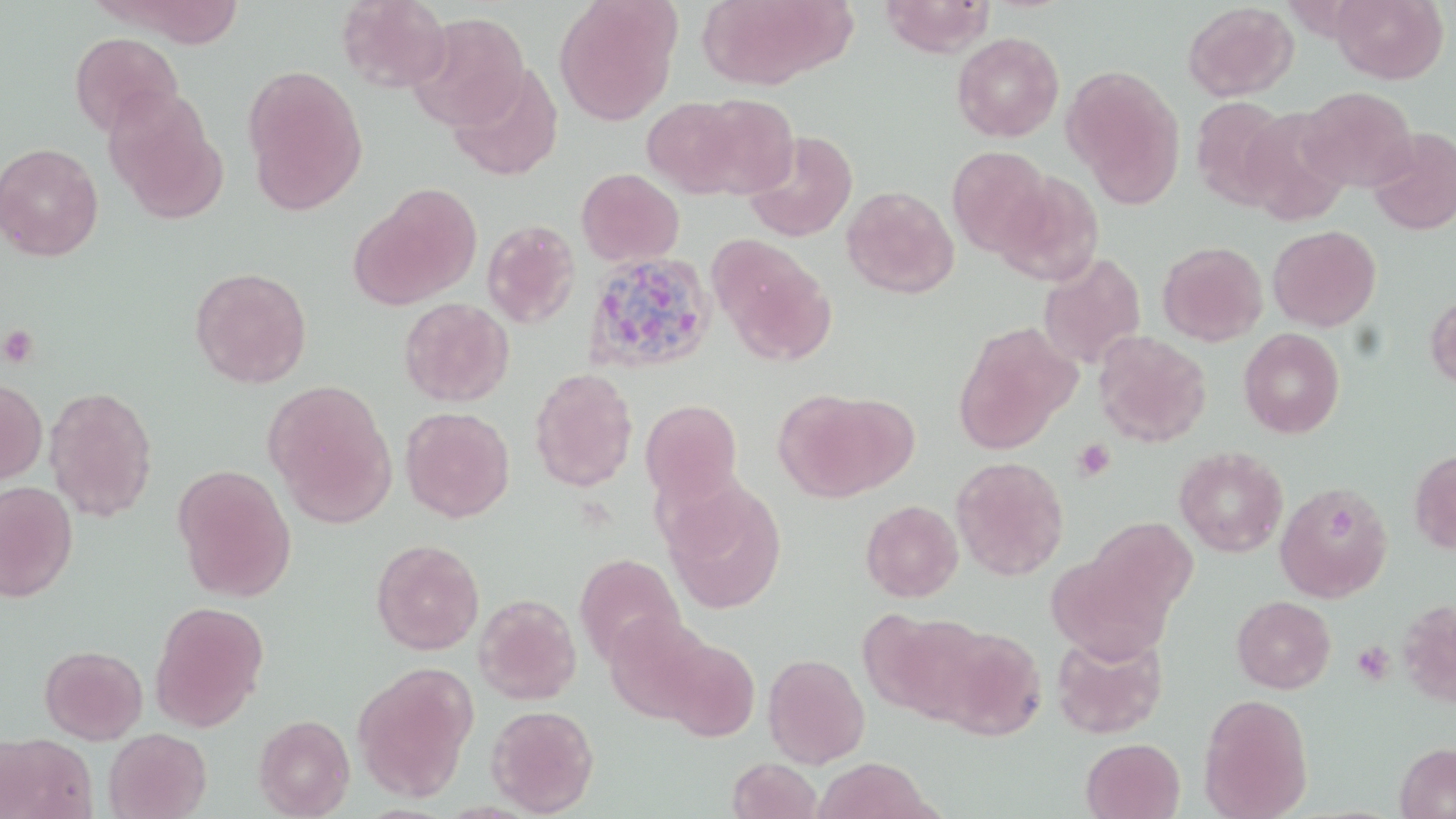

{
  "slide_level_diagnosis": "Plasmodium ovale",
  "platelet_locations": "approximate bounding boxes as (x1,y1)-(x2,y2) corner pairs in pixels: (0,325)-(38,368), (1072,439)-(1115,482), (1351,642)-(1393,685)",
  "stain": "May-Grünwald-Giemsa",
  "magnification": "1000x",
  "modality": "light microscopy",
  "field_of_view": "single",
  "preparation": "thin blood film",
  "image_size": "1456×819 pixels",
  "uninfected_red_blood_cell_locations": "approximate bounding boxes as (x1,y1)-(x2,y2) corner pairs in pixels: (103,0)-(247,48), (336,0)-(452,92), (553,0)-(681,126), (694,0)-(848,89), (880,0)-(996,57), (1331,0)-(1449,85), (1182,2)-(1298,101), (409,11)-(530,132), (70,32)-(183,137), (952,32)-(1064,142), (241,64)-(369,216), (447,64)-(564,182), (1062,64)-(1186,206), (1298,86)-(1418,193), (103,88)-(228,225), (685,94)-(800,198), (639,96)-(754,198), (1190,96)-(1293,209), (1237,108)-(1353,225), (1368,129)-(1456,237), (742,130)-(859,242), (0,142)-(104,261), (945,146)-(1054,259), (576,168)-(684,266), (994,173)-(1104,286), (351,184)-(482,310), (841,185)-(960,299), (481,219)-(582,329), (1267,225)-(1381,332), (707,234)-(834,363), (1157,241)-(1268,346), (1038,253)-(1147,370), (190,266)-(312,389), (1424,290)-(1456,391), (399,296)-(515,407), (952,323)-(1079,454), (1239,327)-(1345,438), (1093,331)-(1213,447), (529,367)-(638,492), (0,377)-(47,488), (263,379)-(399,528), (44,385)-(159,522), (773,389)-(910,502), (640,399)-(743,503), (400,406)-(515,523), (1174,445)-(1289,557), (1409,447)-(1456,554), (950,456)-(1070,581), (171,463)-(297,603), (0,480)-(78,602), (1275,480)-(1394,602), (662,481)-(788,614), (860,499)-(963,602), (1085,517)-(1197,624), (371,539)-(485,655), (1046,552)-(1175,665), (574,554)-(687,668), (474,594)-(582,705), (1231,595)-(1336,694), (1397,598)-(1456,708), (149,600)-(269,732), (859,610)-(988,723), (604,614)-(715,724), (927,623)-(1047,741), (1051,630)-(1168,740), (658,636)-(760,742), (40,645)-(147,744), (763,653)-(870,768), (352,661)-(478,803), (1198,693)-(1314,819), (486,704)-(600,816), (253,714)-(355,818), (104,727)-(212,819), (1,732)-(97,819), (1081,737)-(1185,819), (1394,741)-(1456,819), (727,757)-(822,819), (813,757)-(935,819)",
  "plasmodium_ovale_infected_red_blood_cell_locations": "approximate bounding boxes as (x1,y1)-(x2,y2) corner pairs in pixels: (582,250)-(717,376)"
}